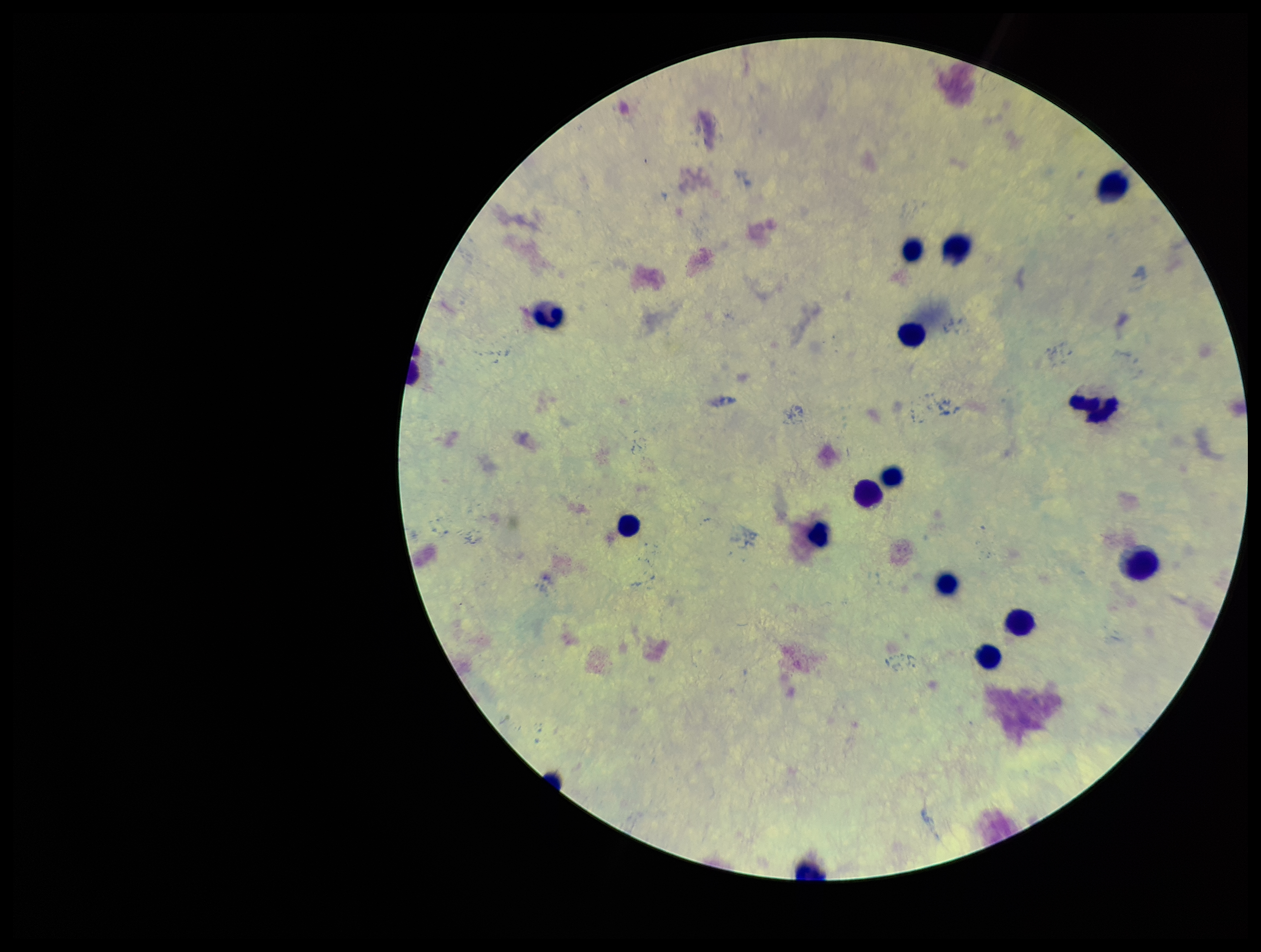
Summary:
  - Preparation: thick smear
  - Patient malaria status: negative
  - Plasmodium parasites: none seen
  - Capture: smartphone photograph through the microscope eyepiece
  - Parasite count: 0
  - Leukocyte count: 14
  - Image size: 1261×952 pixels
  - Stain: Giemsa
  - Field of view: one from this slide